Describe the morphology of the red blood cells.
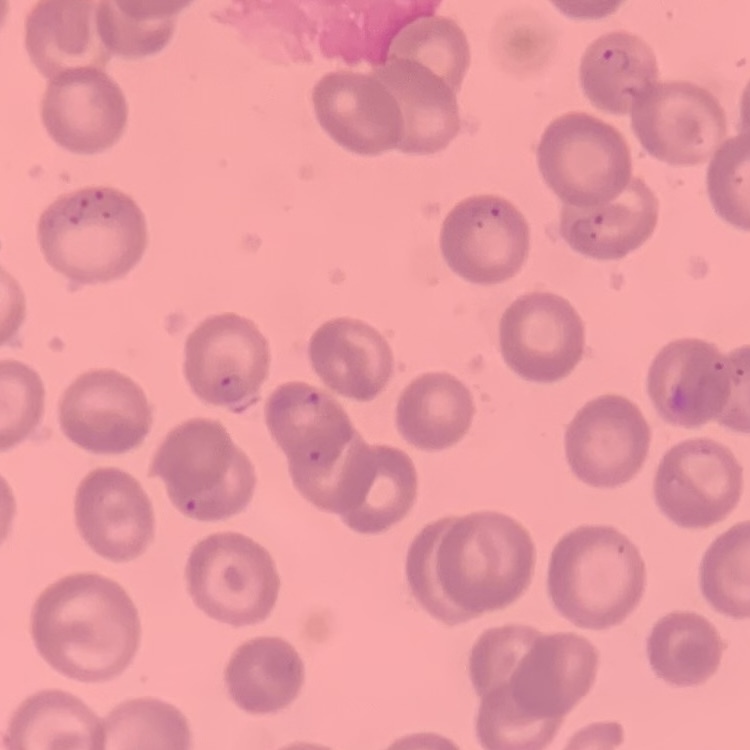
They show no rouleaux formation.

Thin blood film. Field's or Giemsa stain. One tile cut from a larger photomicrograph.